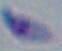
Summary:
  - Identification: Toxoplasma gondii
  - Magnification: 1000x
  - Modality: photomicrograph